Locate every Plasmodium parasite.
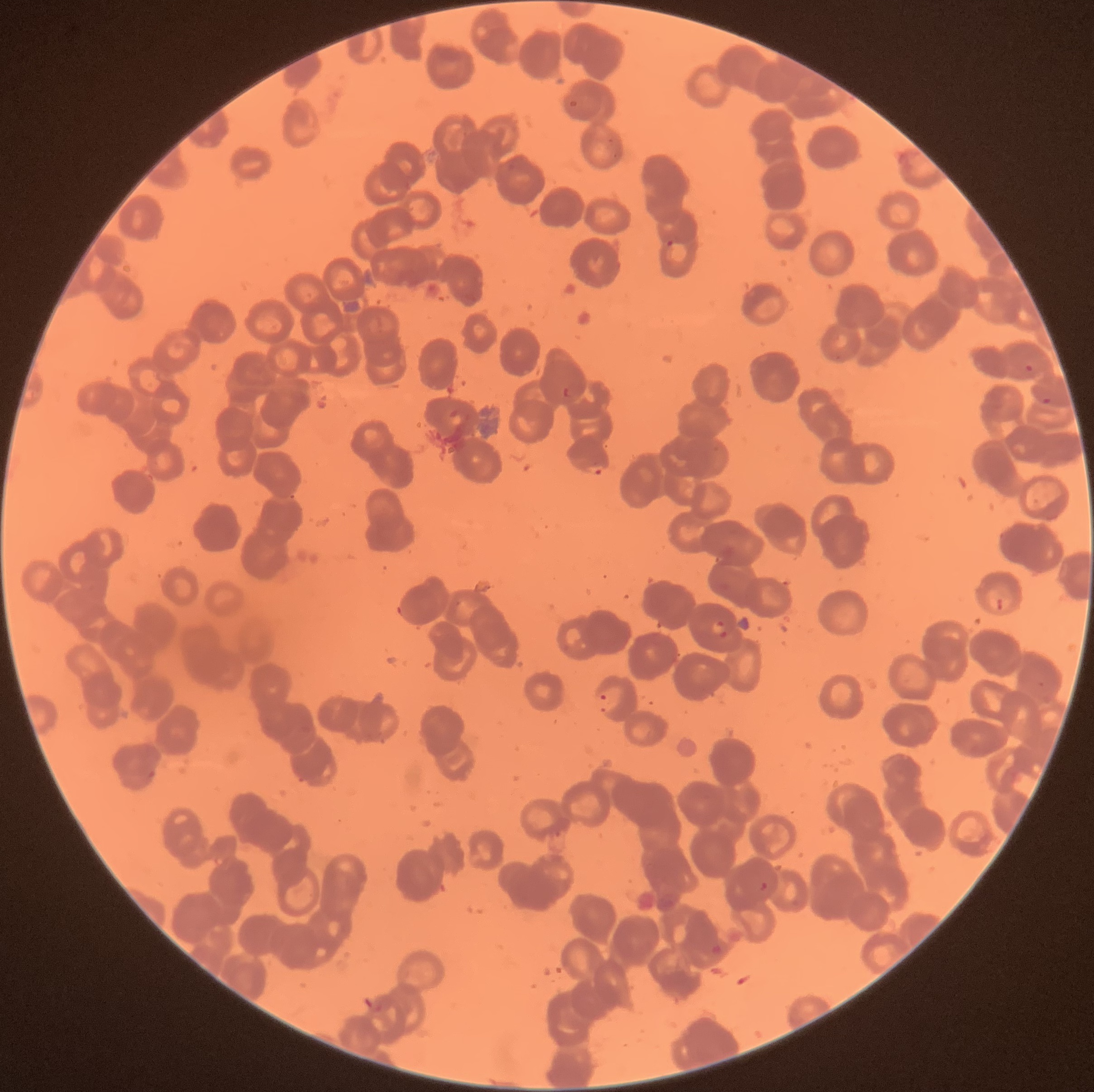
Approximate bounding boxes as named x1/y1/x2/y2 corners in pixels.
Plasmodium parasites: (x1=567, y1=99, x2=579, y2=110), (x1=606, y1=137, x2=620, y2=159), (x1=666, y1=238, x2=691, y2=265), (x1=1025, y1=364, x2=1034, y2=372), (x1=561, y1=385, x2=574, y2=397), (x1=1041, y1=397, x2=1051, y2=406), (x1=587, y1=462, x2=605, y2=477), (x1=995, y1=597, x2=1003, y2=612), (x1=396, y1=603, x2=405, y2=618), (x1=711, y1=616, x2=729, y2=642), (x1=1036, y1=680, x2=1046, y2=689), (x1=597, y1=687, x2=623, y2=714), (x1=147, y1=768, x2=156, y2=779), (x1=759, y1=881, x2=768, y2=892), (x1=708, y1=943, x2=725, y2=957).

{
  "image_size": "1094×1092 pixels",
  "red_blood_cell_morphology": "rouleaux formation",
  "modality": "optical microscopy",
  "preparation": "thin blood film"
}